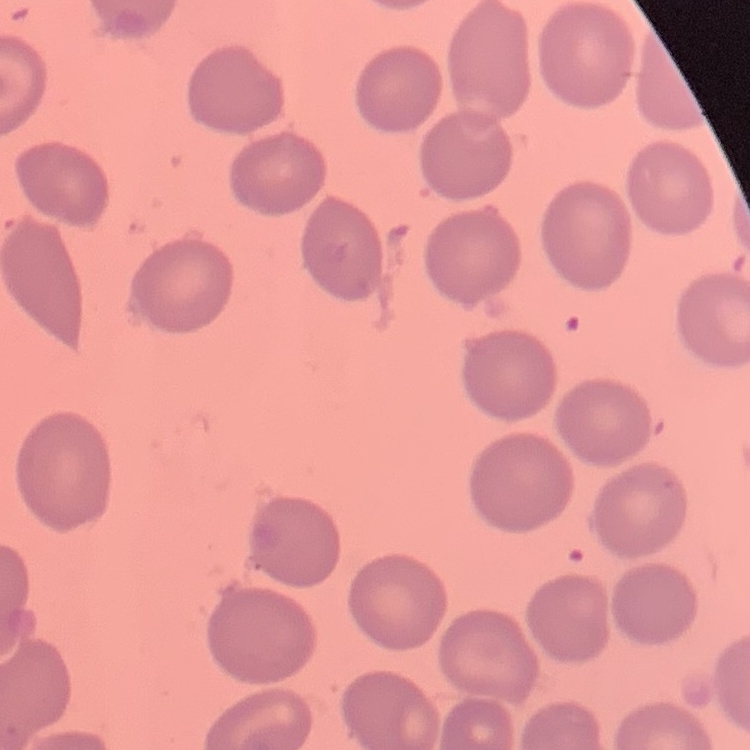
Summary:
  - Red blood cell morphology: no rouleaux formation
  - Preparation: thin blood film
  - Stain: Field's or Giemsa
  - Image type: square crop of a larger photomicrograph